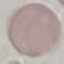

malaria_status: uninfected
preparation: thin blood film
stain: Giemsa
capture: smartphone camera at the microscope eyepiece
image_type: cell patch, automatically extracted from a larger field of view and resized to 64 × 64 pixels